Classify this cell by malaria status.
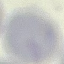

It is uninfected.

Summary:
  - Image type: cell patch, automatically extracted from a larger field of view and resized to 64 × 64 pixels
  - Stain: Giemsa
  - Capture: smartphone camera at the microscope eyepiece
  - Preparation: thin blood film